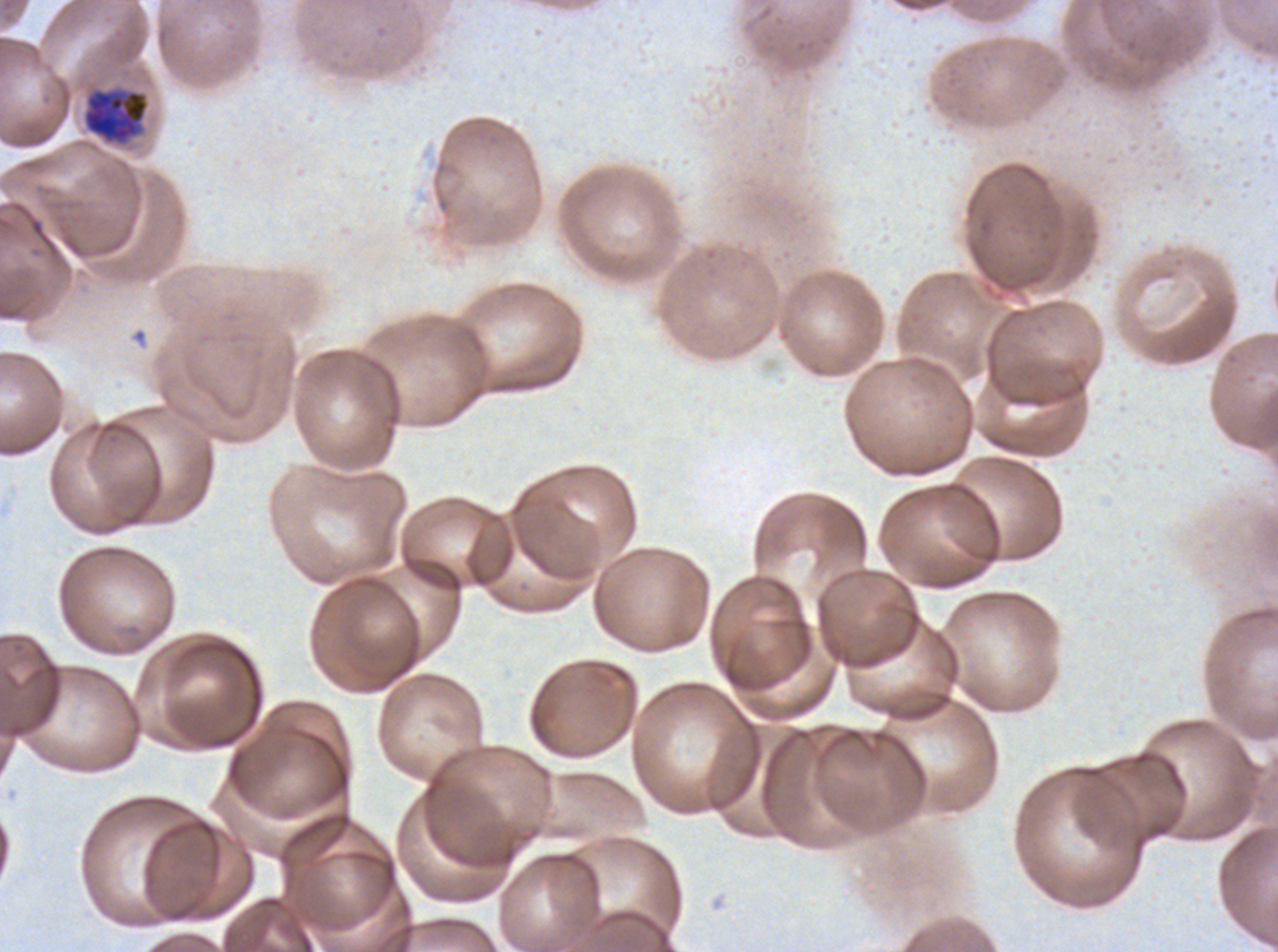

notation = approximate bounding rectangles given as corner coordinates in pixels from the top-left
early schizont locations = (x1=82, y1=88, x2=150, y2=145)
debris locations = (x1=132, y1=328, x2=147, y2=344)
specimen = ex-vivo Plasmodium falciparum culture from a patient in The Gambia, grown for 24 to 48 hours
preparation = thin blood film
field of view = one sub-image of a larger composite
stain = Giemsa
image size = 1278×952 pixels